State which parasite is depicted.
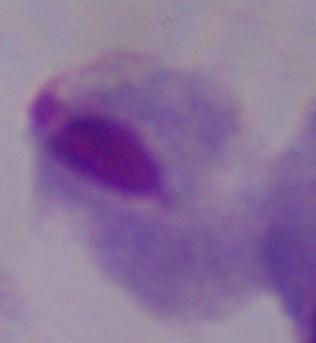
This is a trichomonad.

1000x magnification. Micrograph.